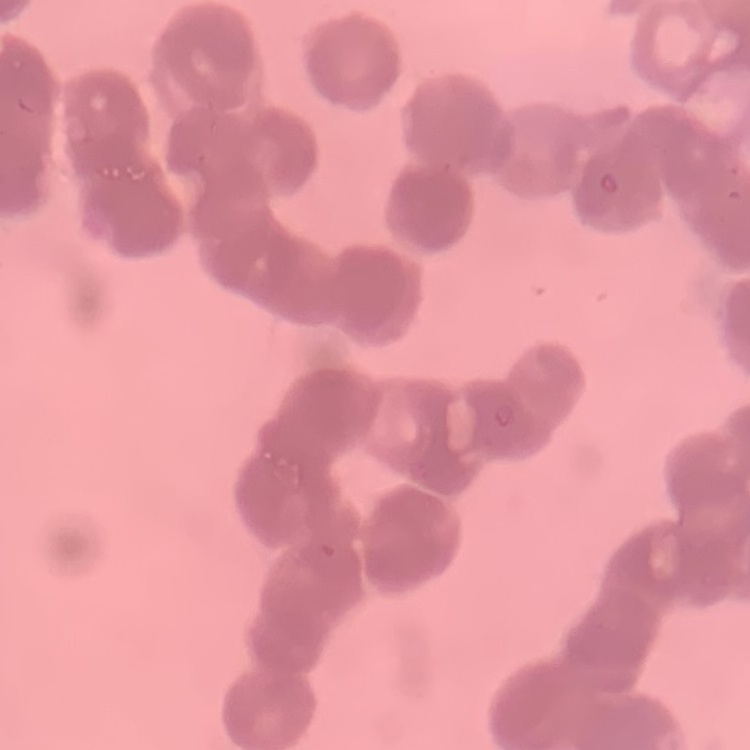
The erythrocytes exhibit rouleaux formation. Square crop of a larger photomicrograph. Thin peripheral smear. Field's or Giemsa stain.